Locate every malaria parasite.
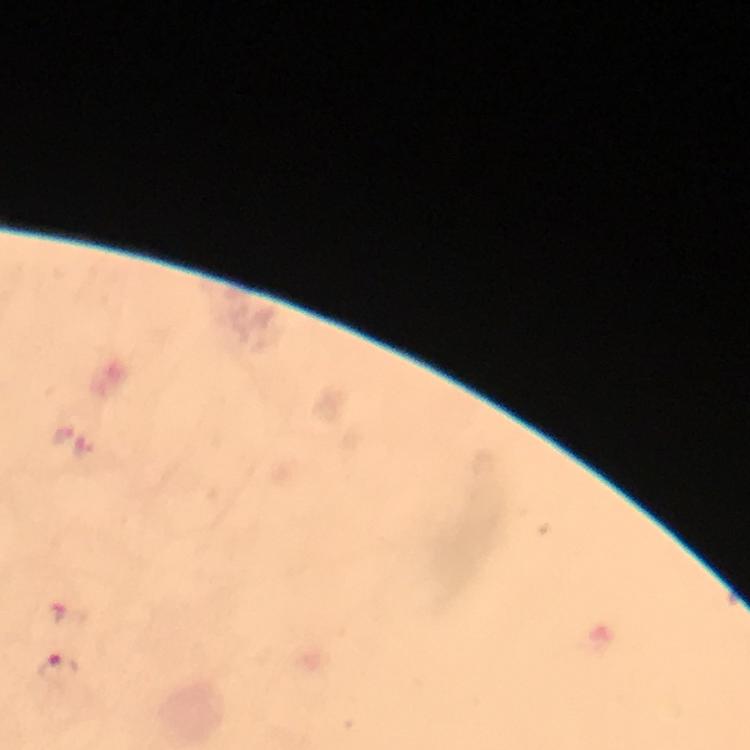

Approximate object centers, in pixels from the top-left corner.
Malaria parasites: (x=59, y=668).

Summary:
  - Immersion oil: applied
  - Preparation: thick blood smear
  - Capture: smartphone mounted on the microscope
  - Magnification: 100x
  - Image size: 750×750 pixels
  - Cropped from: one field of view
  - Stain: Giemsa
  - Context: from a diagnostic examination for malaria